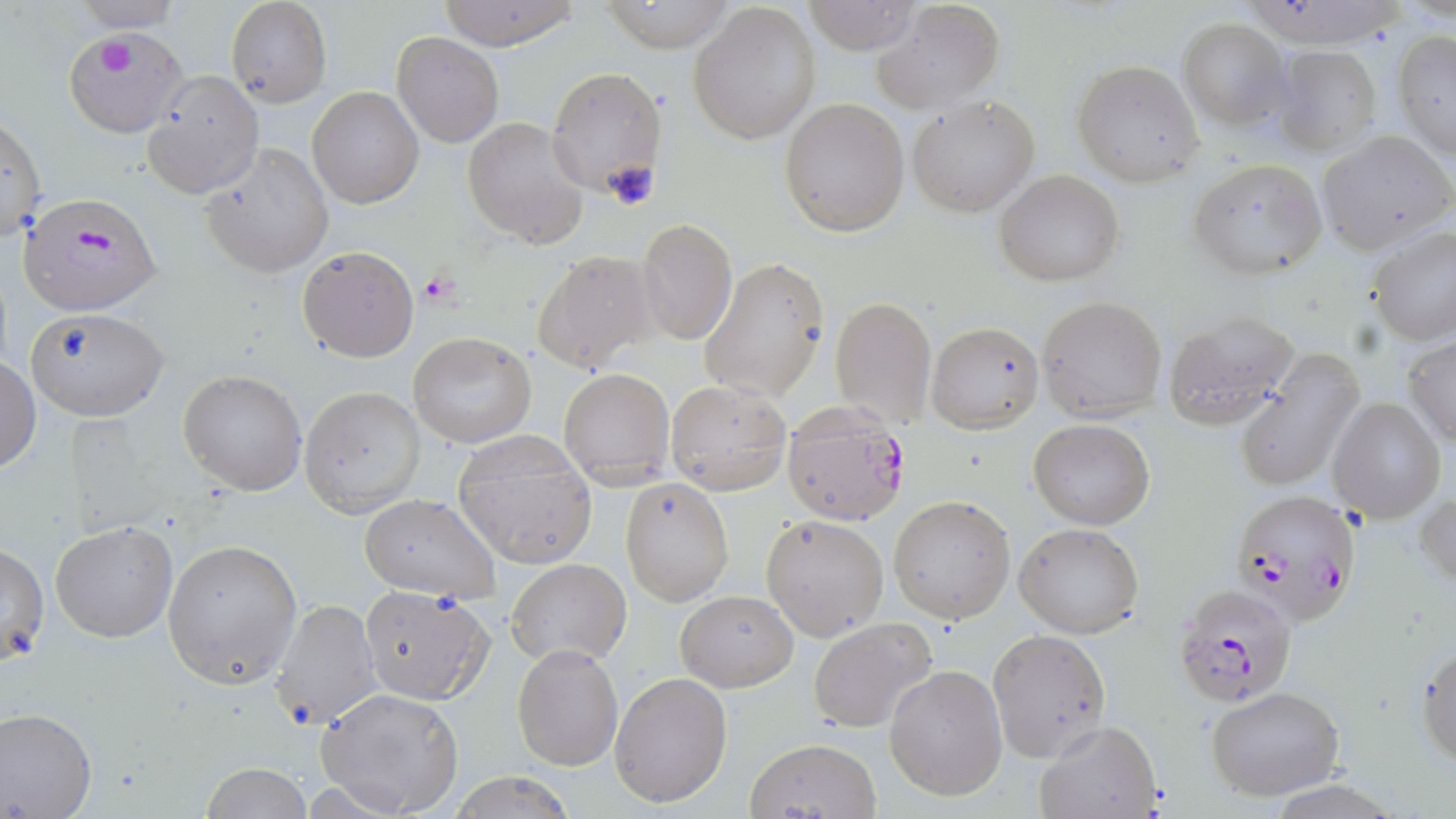
plasmodium_falciparum_infected_red_blood_cell_locations: 'approximate bounding boxes as (x1,y1)-(x2,y2) corner pairs in pixels: (19,185)-(161,311), (780,406)-(913,526), (1231,490)-(1363,624), (1172,581)-(1298,706)'
slide_level_diagnosis: Plasmodium falciparum
image_size: 1456×819 pixels
preparation: thin blood film
uninfected_red_blood_cell_locations: 'approximate bounding boxes as (x1,y1)-(x2,y2) corner pairs in pixels: (226,0)-(330,108), (435,0)-(581,49), (595,0)-(744,52), (69,1)-(187,31), (801,1)-(924,54), (870,1)-(1005,114), (688,2)-(820,144), (1178,18)-(1290,130), (65,28)-(190,136), (1393,29)-(1456,159), (392,32)-(503,146), (1273,45)-(1382,157), (1071,58)-(1206,186), (546,67)-(667,194), (142,69)-(263,199), (307,85)-(424,209), (906,94)-(1041,218), (779,98)-(910,236), (1,113)-(47,244), (462,115)-(590,249), (1318,130)-(1455,255), (202,144)-(334,278), (1188,159)-(1328,279), (994,169)-(1124,286), (635,217)-(738,348), (1366,226)-(1456,346), (296,245)-(421,363), (530,248)-(659,374), (699,257)-(828,402), (1036,295)-(1167,422), (830,297)-(936,427), (25,308)-(170,421), (1161,310)-(1299,431), (925,320)-(1044,432), (408,332)-(537,448), (1403,334)-(1456,449), (1232,354)-(1363,492), (1,355)-(40,475), (558,367)-(674,490), (177,370)-(308,494), (665,379)-(791,494), (299,386)-(425,514), (1328,396)-(1446,523), (1029,418)-(1155,529), (453,435)-(597,567), (620,477)-(734,605), (1415,489)-(1456,592), (357,494)-(501,603), (889,495)-(1016,624), (760,514)-(891,641), (50,521)-(178,643), (1013,523)-(1145,638), (162,538)-(302,688), (1,543)-(49,667), (506,558)-(632,667), (359,586)-(494,704), (676,590)-(799,692), (268,598)-(382,732), (807,618)-(938,733), (986,629)-(1111,761), (1416,638)-(1456,768), (513,644)-(622,770), (884,664)-(1008,801), (611,672)-(732,806), (1204,685)-(1347,801), (314,687)-(464,817), (0,706)-(98,818), (1032,721)-(1163,819), (744,737)-(882,817), (201,763)-(312,819), (441,772)-(583,818)'
magnification: 1000x
modality: optical microscopy
platelet_locations: 'approximate bounding boxes as (x1,y1)-(x2,y2) corner pairs in pixels: (87,34)-(148,81), (602,158)-(659,214), (420,270)-(462,306)'
stain: May-Grünwald-Giemsa
field_of_view: one of a larger specimen